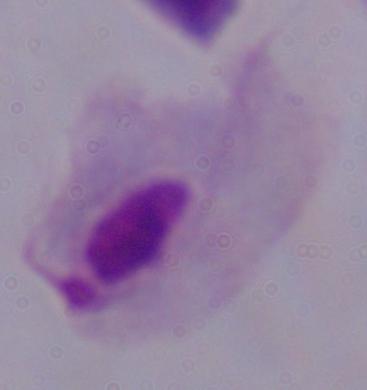
Captured at 1000x magnification. Micrograph. A trichomonad is seen.